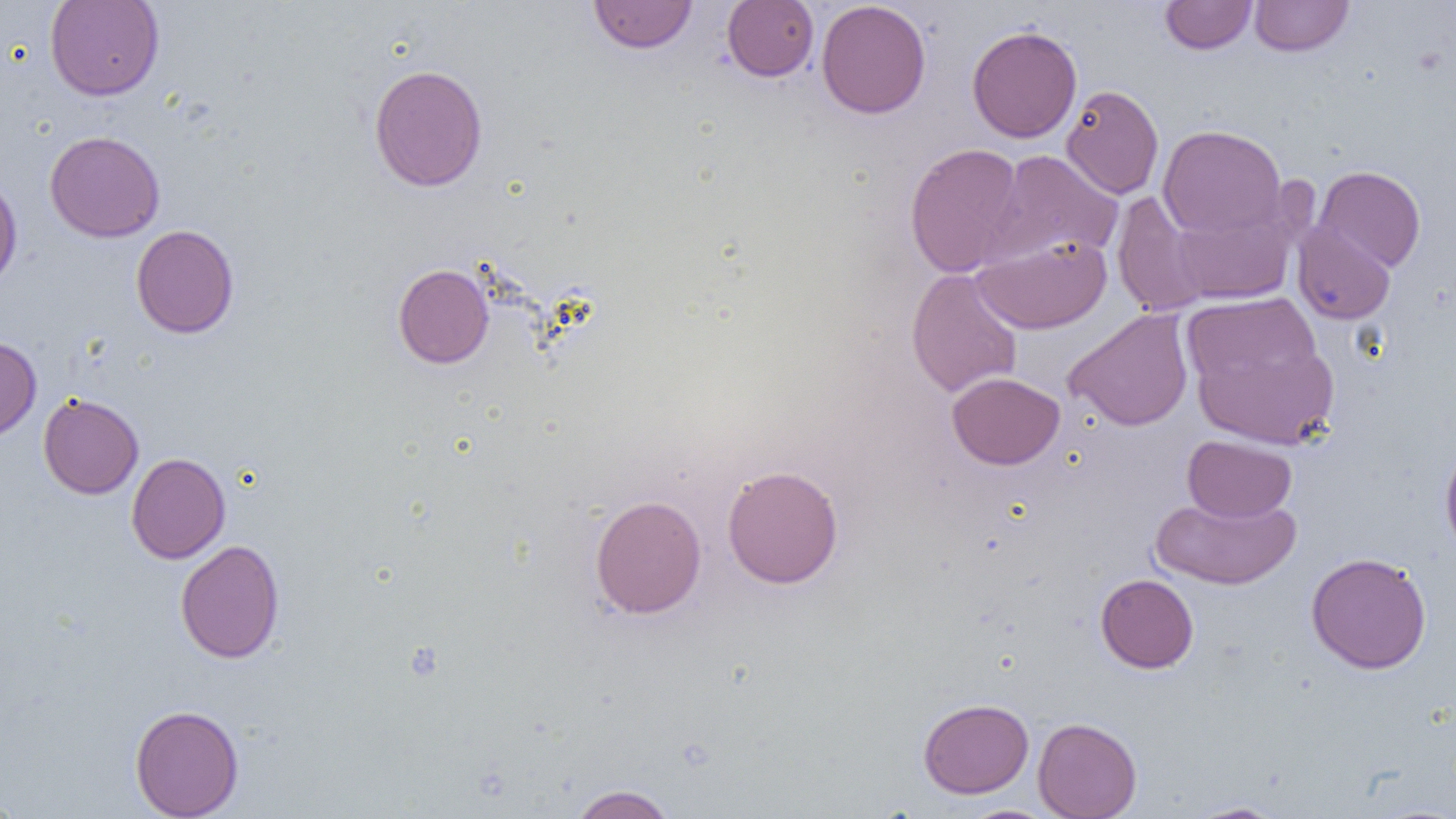
Approximate bounding boxes as (x1, y1, x2, y2) in pixels. Uninfected red blood cell locations: (45, 0, 164, 101), (588, 0, 698, 54), (722, 0, 819, 82), (815, 0, 931, 119), (1160, 0, 1257, 54), (1249, 0, 1354, 57), (966, 24, 1082, 143), (368, 63, 488, 192), (1061, 84, 1164, 199), (1157, 124, 1287, 240), (44, 130, 165, 243), (904, 142, 1027, 278), (986, 149, 1124, 266), (1313, 165, 1426, 273), (0, 174, 22, 290), (1112, 191, 1210, 316), (1170, 201, 1298, 305), (1292, 221, 1396, 325), (131, 224, 239, 338), (972, 235, 1111, 334), (393, 264, 494, 368), (906, 268, 1023, 397), (1183, 292, 1322, 393), (1064, 308, 1194, 431), (0, 336, 41, 442), (1193, 338, 1338, 449), (947, 371, 1065, 470), (38, 393, 144, 499), (1182, 435, 1297, 522), (1440, 439, 1456, 562), (126, 452, 231, 563), (722, 464, 844, 589), (1150, 492, 1301, 589), (589, 494, 707, 619), (175, 539, 285, 663), (1305, 551, 1432, 674), (1095, 573, 1199, 673), (918, 698, 1034, 798), (129, 704, 244, 818), (1033, 717, 1142, 818), (568, 784, 678, 819), (0, 792, 23, 818), (1183, 800, 1292, 818), (958, 805, 1059, 819). Slide-level diagnosis: no evidence of blood parasites. Captured at 1000x magnification. Image is 1456×819 pixels. Optical microscopy. Single field of view. Thin blood smear.